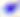

{
  "magnification": "400x",
  "identification": "Toxoplasma gondii",
  "modality": "photomicrograph"
}